Look for Plasmodium parasites.
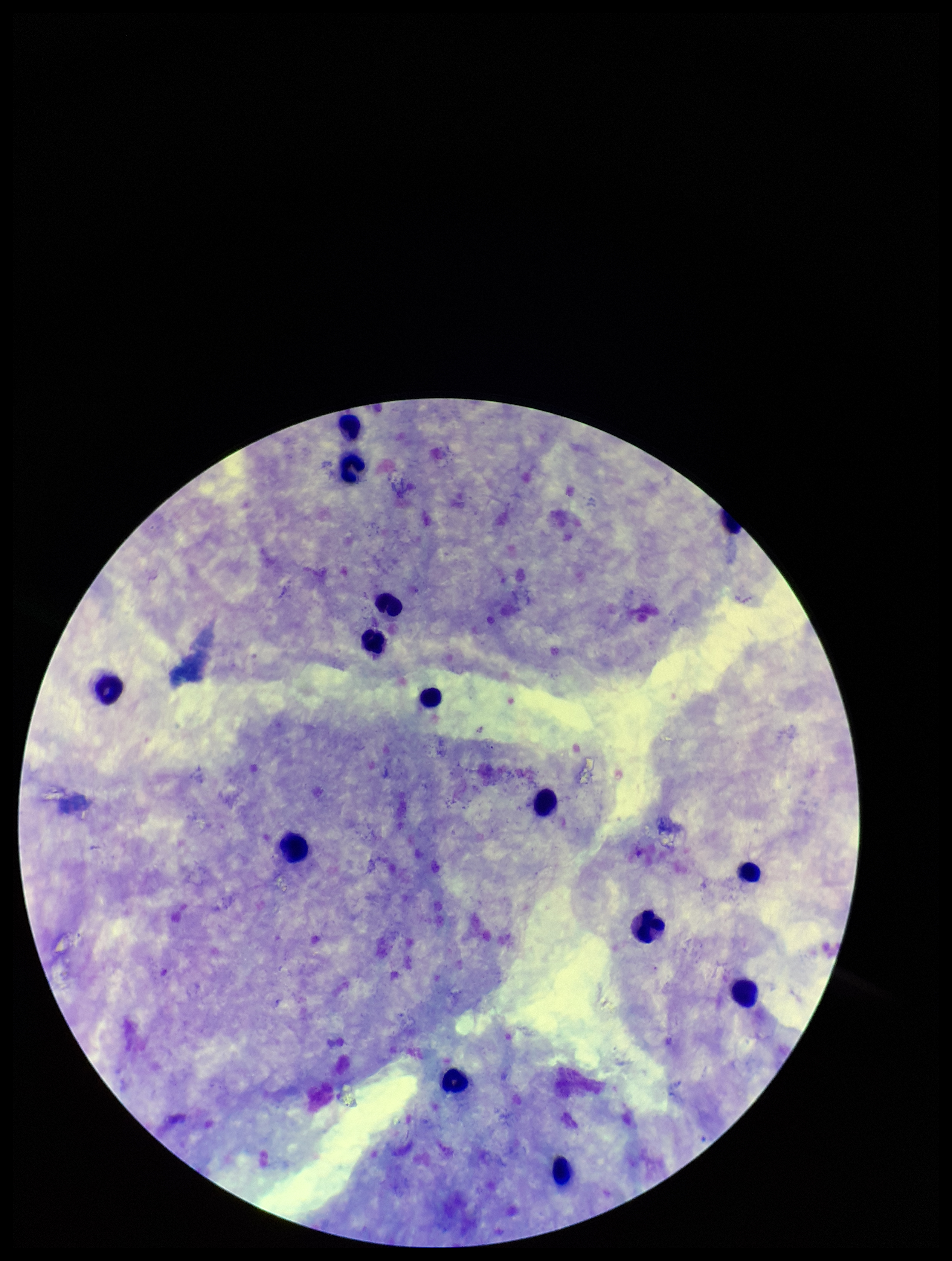
None identified.

Summary:
  - Leukocyte count: 13
  - Parasite count: 0
  - Field of view: one from this slide
  - Stain: Giemsa
  - Image size: 952×1261 pixels
  - Patient malaria status: negative
  - Preparation: thick smear
  - Capture: smartphone photograph through the microscope eyepiece